Report the malaria status.
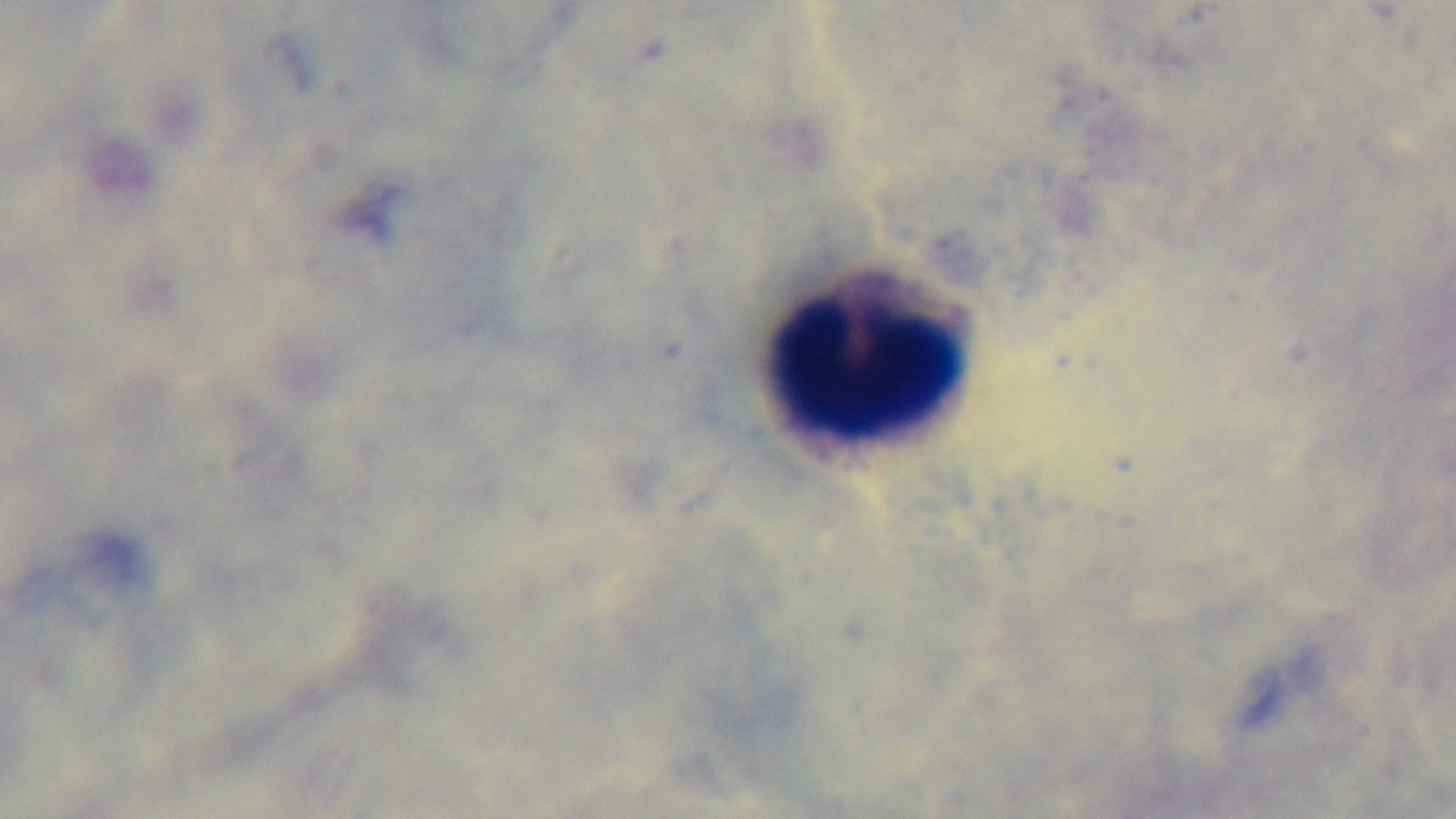

Negative.

Summary:
  - Modality: light microscopy
  - Preparation: thick
  - Field of view: one from the slide
  - Capture: mounted 4K digital camera
  - Stain: Giemsa
  - Objective: 100x oil immersion